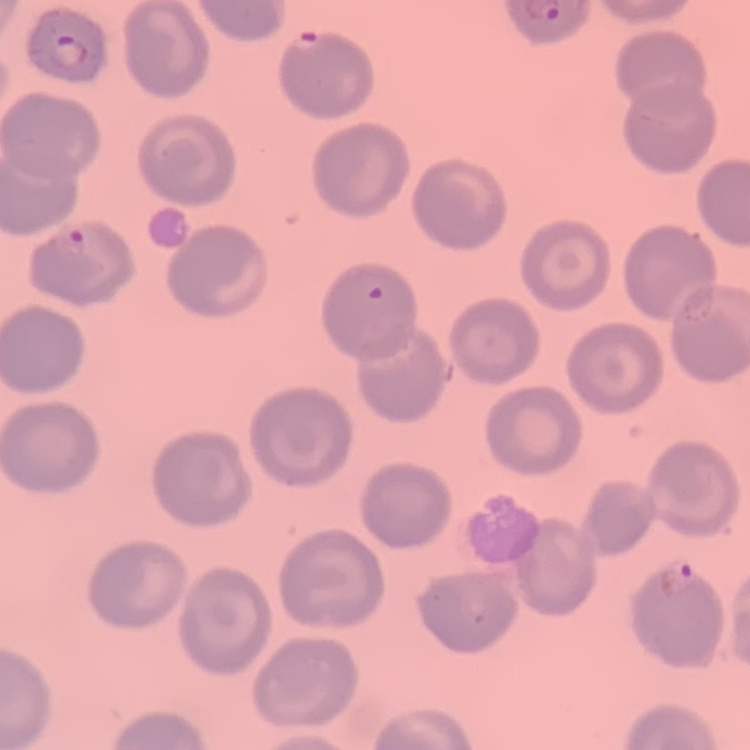

The red blood cells exhibit no rouleaux formation. Field's or Giemsa stain. One tile cut from a larger photomicrograph. Thin blood smear.